State which parasite is depicted.
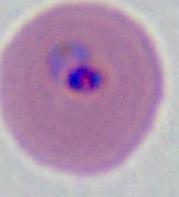

This is Plasmodium.

modality: photomicrograph
magnification: 400x or 1000x